Classify this cell by malaria status.
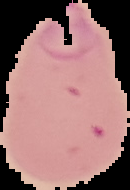

Parasitized.

{
  "image_type": "segmented cell region with the area outside set to black",
  "preparation": "thin blood film",
  "image_size": "130×190 pixels"
}